Classify this cell by malaria status.
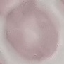

It is uninfected.

Automatically extracted cell patch, resized to 64 × 64 pixels. Giemsa-stained preparation. Thin blood smear. Acquired by smartphone through the microscope eyepiece.